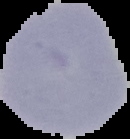

Summary:
  - Image type: segmented cell region with the area outside set to black
  - Malaria status: uninfected
  - Preparation: thin blood film
  - Image size: 130×139 pixels